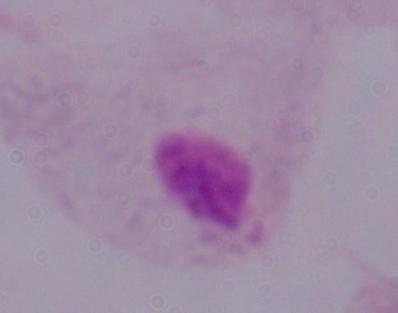

Summary:
  - Identification: trichomonad
  - Magnification: 1000x
  - Modality: micrograph